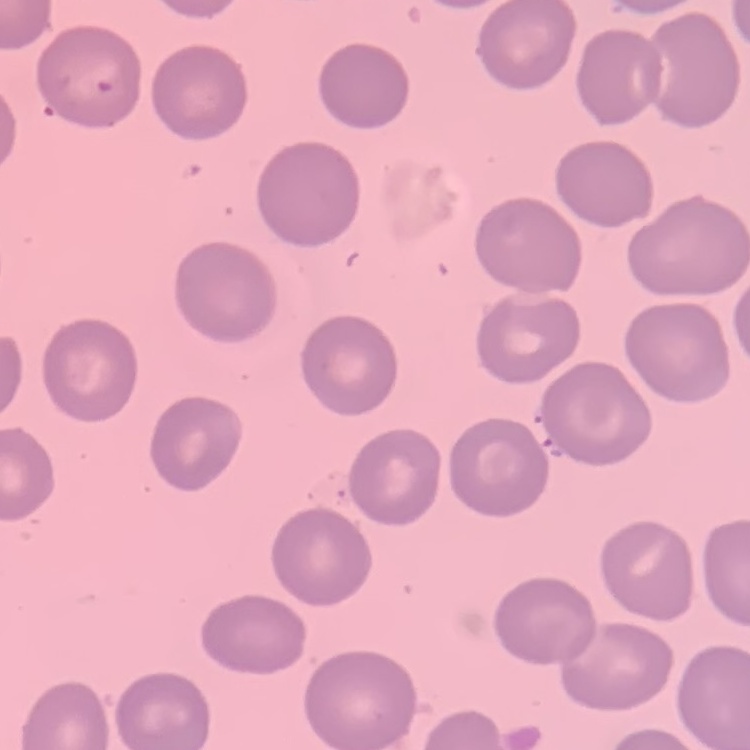
Summary:
  - Erythrocyte morphology: no rouleaux formation
  - Stain: Field's or Giemsa
  - Preparation: thin blood film
  - Image type: square crop of a larger photomicrograph